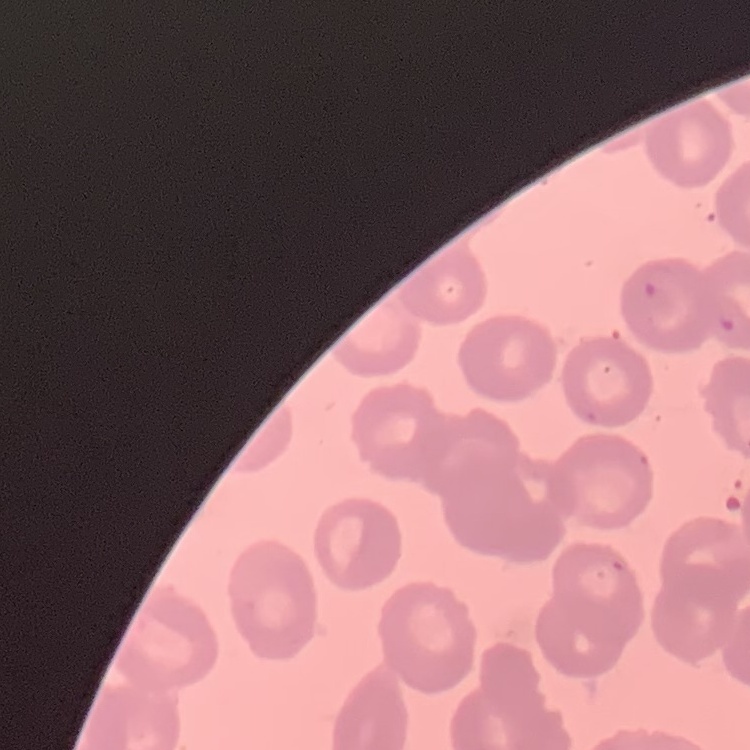
red blood cell morphology = no rouleaux formation
image type = square crop of a larger photomicrograph
preparation = thin peripheral smear
stain = Field's or Giemsa